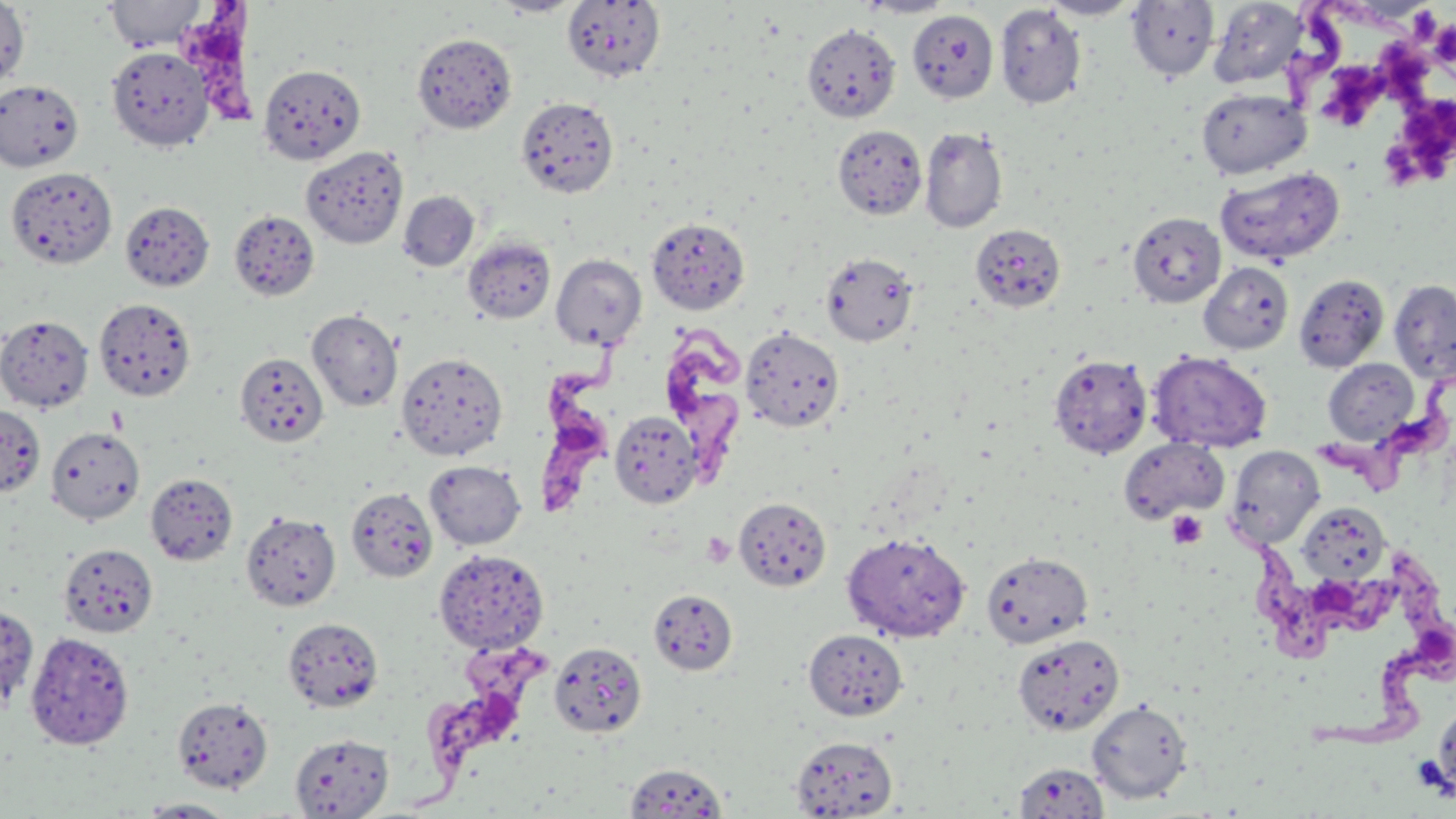
slide-level diagnosis = Trypanosoma brucei
field of view = single
preparation = thin blood film
platelet locations = approximate bounding boxes as [x1, y1, x2, y2] in pixels: [1375, 35, 1436, 101], [1331, 65, 1388, 136], [1381, 97, 1456, 183], [1166, 510, 1208, 549], [702, 532, 735, 567]
image size = 1456×819 pixels
uninfected red blood cell locations = approximate bounding boxes as [x1, y1, x2, y2] in pixels: [0, 0, 30, 92], [104, 0, 206, 51], [491, 0, 583, 17], [859, 0, 955, 18], [1039, 0, 1142, 20], [562, 1, 665, 82], [1126, 1, 1220, 81], [1208, 1, 1311, 90], [994, 4, 1087, 109], [907, 10, 998, 104], [802, 23, 901, 122], [412, 32, 517, 133], [106, 46, 214, 151], [258, 63, 366, 165], [0, 79, 84, 172], [1195, 87, 1311, 179], [516, 96, 619, 198], [832, 124, 927, 220], [919, 127, 1008, 233], [300, 146, 409, 249], [1215, 166, 1345, 266], [6, 167, 117, 269], [399, 191, 479, 270], [120, 201, 215, 291], [229, 209, 320, 302], [1127, 211, 1226, 308], [646, 217, 750, 315], [970, 223, 1065, 313], [462, 236, 556, 323], [820, 252, 919, 347], [551, 254, 647, 350], [1199, 261, 1294, 354], [1293, 273, 1390, 372], [1389, 278, 1456, 382], [93, 297, 197, 402], [306, 308, 403, 412], [0, 314, 94, 413], [741, 328, 844, 433], [1147, 351, 1272, 453], [234, 352, 328, 448], [396, 352, 508, 461], [1048, 354, 1153, 459], [1323, 358, 1419, 446], [0, 405, 45, 497], [609, 411, 702, 508], [46, 427, 144, 525], [1119, 438, 1229, 523], [1224, 445, 1325, 548], [424, 460, 527, 550], [145, 472, 237, 565], [346, 488, 438, 583], [733, 497, 831, 593], [1296, 502, 1390, 583], [240, 511, 341, 612], [842, 532, 970, 642], [58, 543, 157, 637], [434, 549, 549, 653], [981, 551, 1093, 649], [648, 589, 738, 675], [0, 603, 38, 712], [283, 618, 383, 712], [803, 629, 908, 721], [25, 631, 135, 750], [1012, 633, 1125, 736], [549, 641, 647, 738], [171, 695, 274, 794], [1432, 698, 1456, 804], [1087, 700, 1192, 804], [290, 733, 394, 818], [789, 736, 897, 817], [623, 762, 729, 818], [1013, 762, 1109, 817], [136, 798, 239, 817]
Trypanosoma brucei locations = approximate bounding boxes as [x1, y1, x2, y2] in pixels: [173, 2, 273, 137], [665, 309, 760, 489], [535, 338, 638, 526], [1312, 380, 1453, 498], [1224, 519, 1401, 675], [1304, 547, 1456, 750], [410, 639, 563, 817]
stain = May-Grünwald-Giemsa
modality = optical microscopy
magnification = 1000x